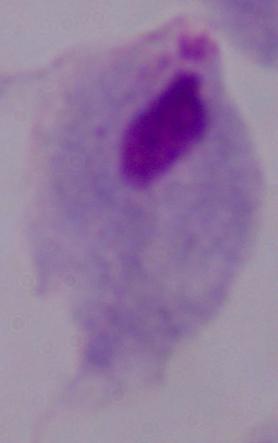

1000x magnification. A trichomonad is seen. Micrograph.